Give the position of every leukocyte visible.
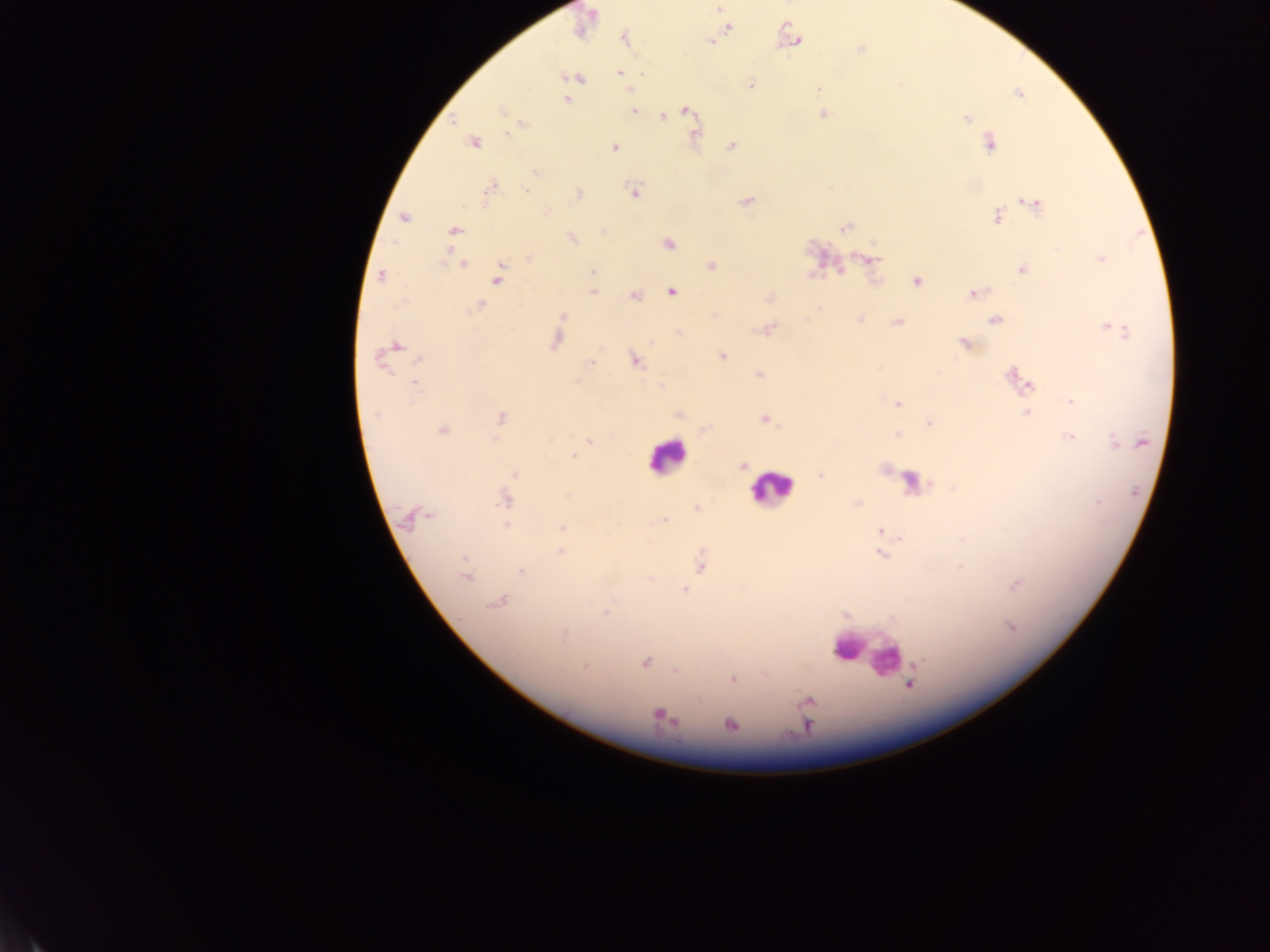
Approximate centers as [x, y] in pixels.
Leukocytes: [666, 456], [911, 483], [773, 487], [848, 647], [869, 653], [886, 660].

image size = 1270×952 pixels
field of view = single
malaria parasite locations = approximate centers as [x, y] in pixels: [719, 9], [726, 28], [624, 37], [709, 41], [796, 41], [861, 49], [620, 73], [571, 77], [750, 85], [820, 89], [631, 91], [1018, 93], [567, 97], [567, 99], [632, 110], [685, 110], [502, 111], [822, 114], [661, 116], [967, 119], [453, 121], [520, 123], [473, 142], [989, 143], [732, 146], [614, 147], [491, 187], [634, 192], [578, 194], [745, 201], [1033, 203], [996, 216], [403, 217], [845, 227], [454, 230], [571, 239], [667, 242], [529, 258], [869, 259], [1100, 259], [461, 263], [710, 265], [1022, 269], [591, 272], [380, 275], [499, 275], [916, 281], [671, 290], [593, 291], [975, 293], [634, 295], [770, 297], [479, 306], [563, 315], [860, 319], [996, 319], [897, 321], [558, 327], [767, 328], [1109, 328], [679, 332], [556, 339], [964, 343], [393, 348], [384, 356], [721, 356], [633, 359], [590, 360], [417, 361], [759, 374], [1012, 375], [414, 384], [1026, 385], [659, 386], [1071, 401], [898, 404], [1026, 412], [678, 415], [500, 417], [764, 418], [928, 423], [704, 429], [442, 430], [898, 434], [1070, 436], [591, 440], [574, 456], [742, 465], [884, 469], [515, 473], [821, 474], [954, 487], [505, 499], [857, 503], [696, 508], [413, 516], [662, 521], [506, 527], [561, 528], [881, 531], [559, 551], [881, 553], [464, 562], [700, 563], [521, 570], [466, 575], [1015, 584], [685, 590], [498, 602], [606, 614], [845, 614], [563, 633], [646, 662], [584, 666], [675, 670], [732, 678], [808, 701], [660, 715], [730, 724]
preparation = thick blood smear
capture = mobile-phone photograph through a microscope
country = Ghana